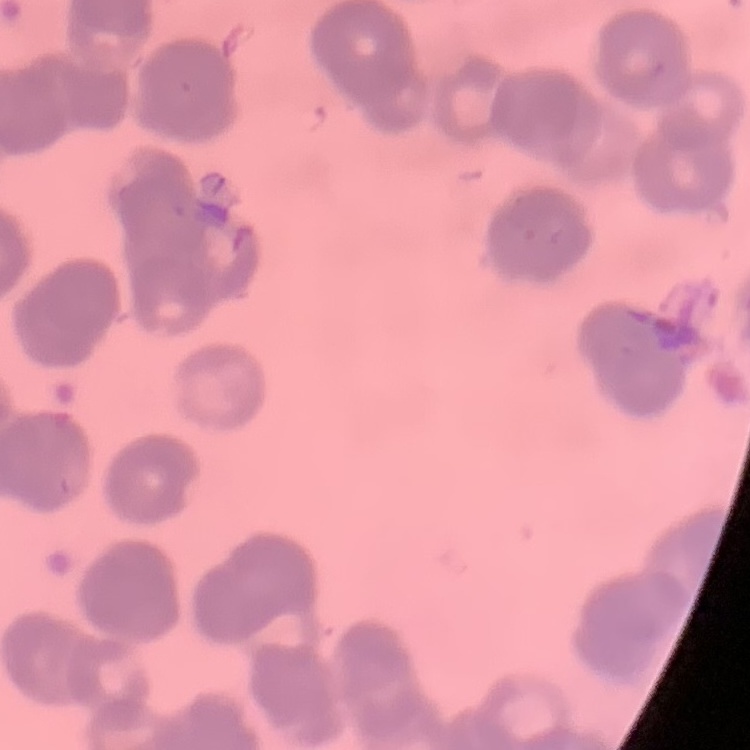 The erythrocytes exhibit rouleaux formation. Thin blood smear. One tile cut from a larger photomicrograph. Stained with either Field's or Giemsa.